State the blood parasite species.
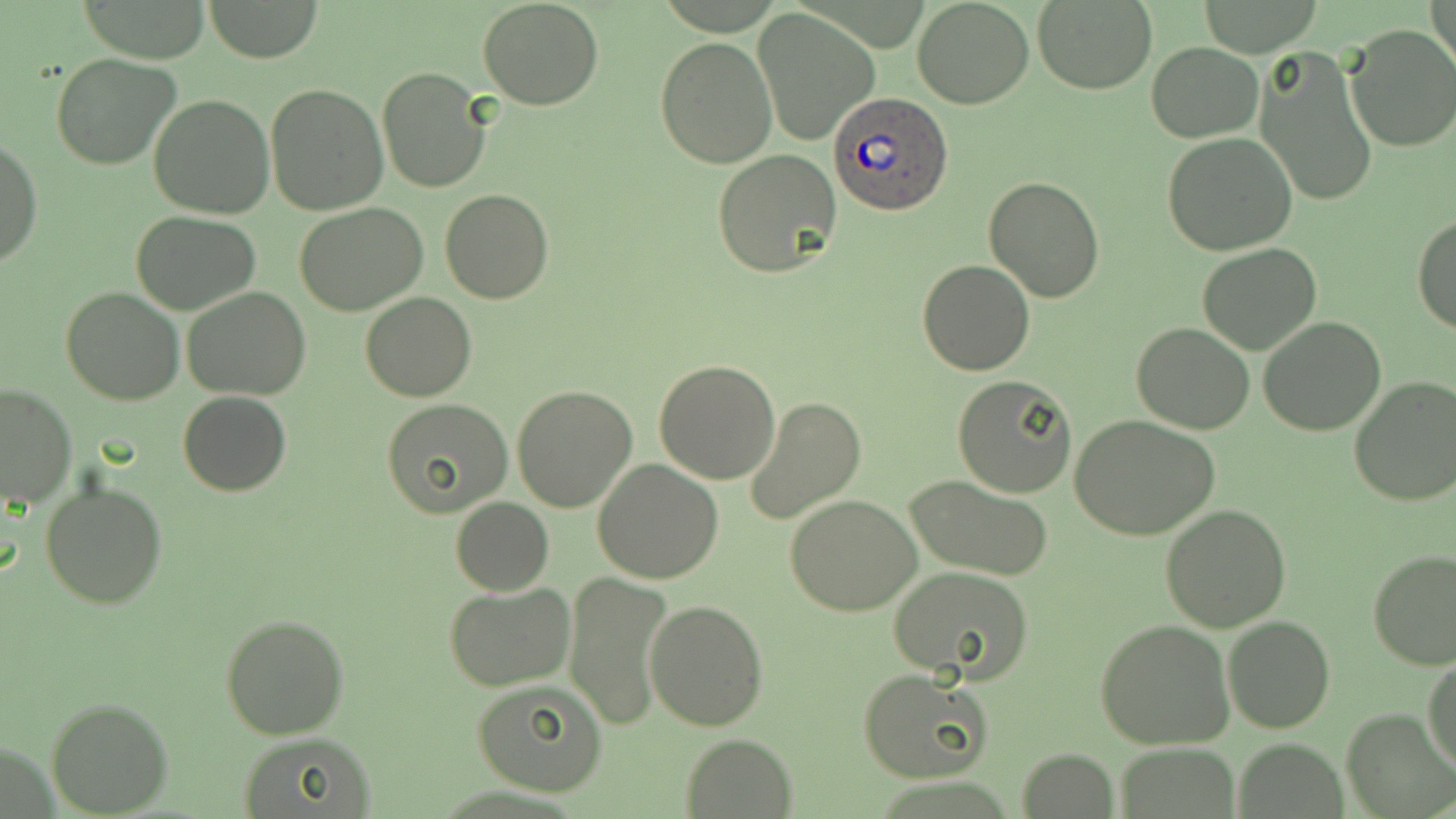

Plasmodium ovale.

Approximate bounding boxes as (x1,y1)-(x2,y2) corner pairs in pixels. Uninfected red blood cell locations: (79,0)-(212,62), (201,0)-(325,64), (912,0)-(1034,110), (1033,0)-(1156,93), (477,1)-(604,110), (1430,1)-(1456,73), (753,8)-(879,145), (1343,22)-(1456,154), (655,37)-(778,170), (1146,41)-(1264,143), (1255,48)-(1379,206), (51,51)-(180,169), (377,67)-(490,192), (264,83)-(389,216), (148,94)-(275,220), (1161,134)-(1298,257), (1,135)-(40,270), (713,149)-(842,280), (983,175)-(1105,302), (440,189)-(554,305), (294,204)-(426,316), (131,211)-(260,314), (1413,216)-(1456,336), (1196,242)-(1321,355), (917,257)-(1035,376), (60,286)-(184,405), (183,286)-(312,400), (360,293)-(477,402), (1258,317)-(1387,437), (1132,323)-(1255,436), (654,359)-(780,484), (951,375)-(1077,496), (1349,378)-(1456,507), (0,382)-(76,507), (511,385)-(638,513), (177,392)-(291,496), (744,396)-(867,525), (381,398)-(513,516), (1069,415)-(1220,540), (593,458)-(725,585), (905,474)-(1056,581), (40,480)-(167,609), (784,494)-(922,616), (450,498)-(554,594), (1160,504)-(1290,631), (1367,549)-(1456,671), (887,565)-(1035,683), (563,570)-(675,732), (444,585)-(575,692), (643,598)-(770,731), (219,613)-(349,740), (1222,615)-(1335,733), (1095,620)-(1234,749), (1424,655)-(1456,774), (860,669)-(990,782), (468,680)-(608,796), (46,697)-(172,817), (1343,708)-(1454,817), (236,733)-(377,816), (679,734)-(799,817), (1235,739)-(1347,816), (1116,743)-(1240,818), (1016,748)-(1117,818). Plasmodium ovale-infected red blood cell locations: (828,93)-(953,218). Thin blood film. 1000x magnification. May-Grünwald-Giemsa-stained preparation. Optical microscopy. Image is 1456×819 pixels. Single field of view.